Classify this cell by malaria status.
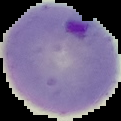
It is parasitized.

image size = 121×121 pixels
image type = segmented cell region with the area outside set to black
preparation = thin blood smear